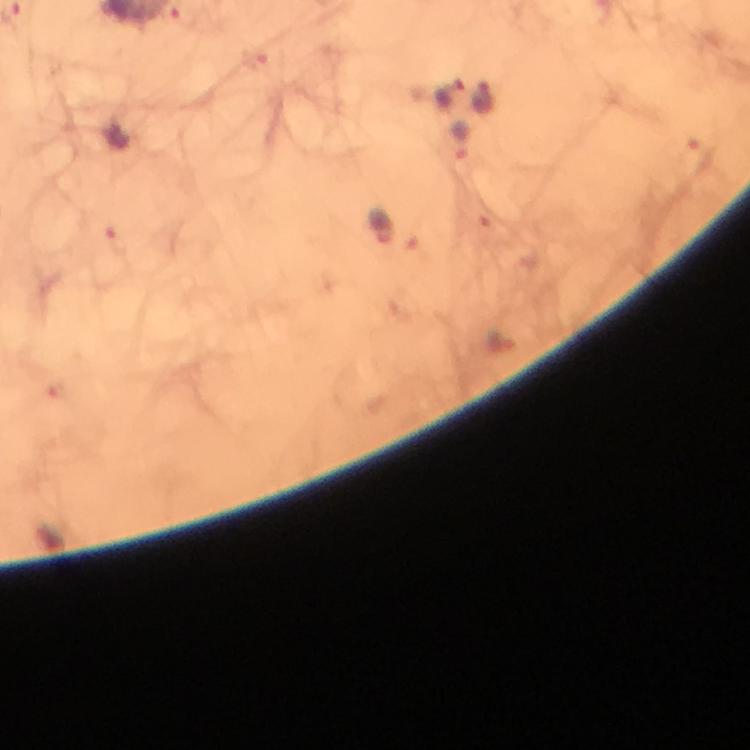

preparation = thick blood smear
immersion oil = applied
capture = smartphone camera through the microscope
image size = 750×750 pixels
malaria parasite locations = approximate object centers, in pixels from the top-left corner: (x=447, y=94), (x=485, y=99), (x=464, y=139), (x=383, y=226)
context = from a malaria diagnostic workup
stain = Giemsa
magnification = 100x
cropped from = one field of view